Comment on the morphology of the red blood cells.
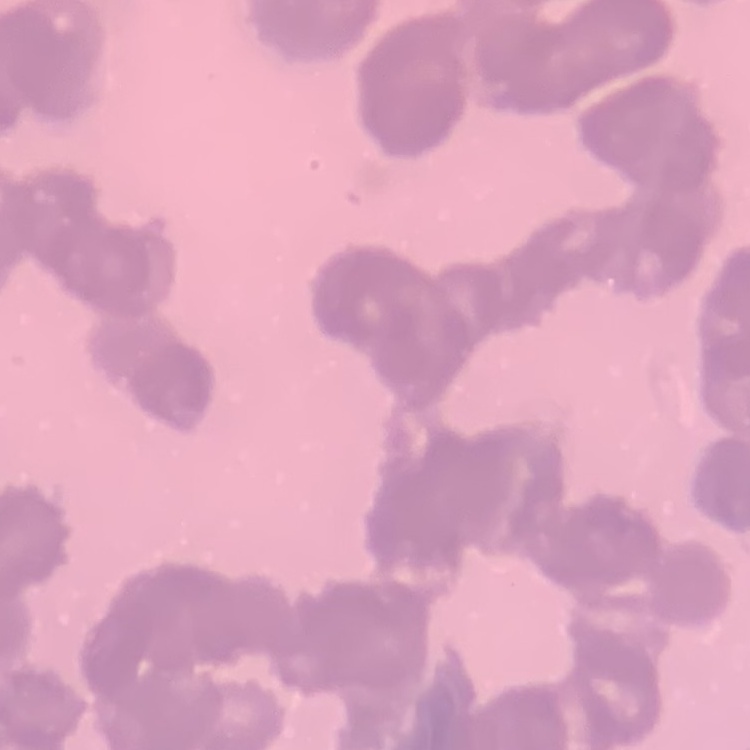
They show rouleaux formation.

stain = Field's or Giemsa
image type = square crop of a larger photomicrograph
preparation = thin blood film